Identify the blood parasite species.
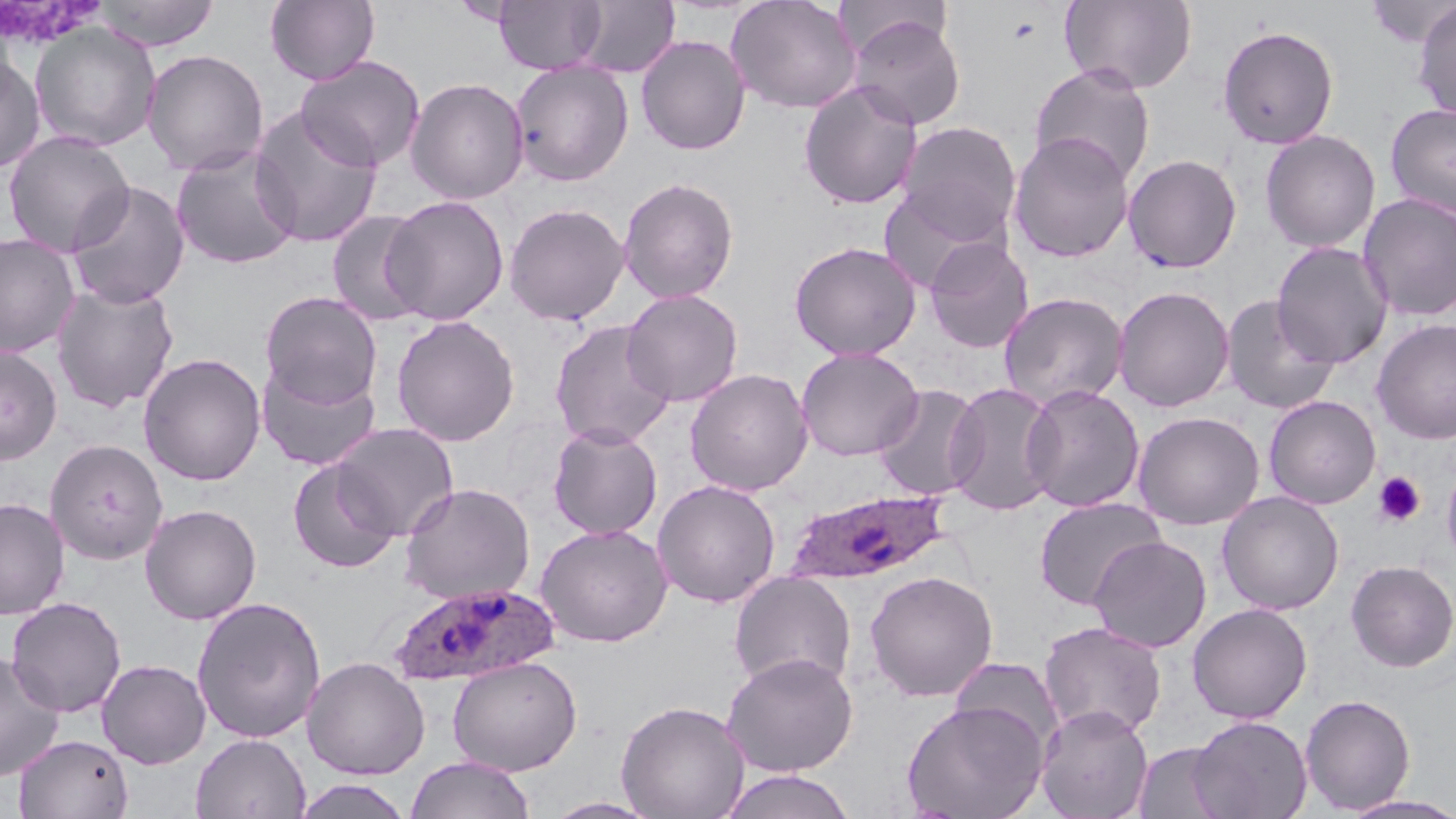
Plasmodium ovale.

{
  "field_of_view": "one of a larger specimen",
  "platelet_locations": "approximate bounding boxes as (x1,y1)-(x2,y2) corner pairs in pixels: (1373,472)-(1426,527)",
  "magnification": "1000x",
  "uninfected_red_blood_cell_locations": "approximate bounding boxes as (x1,y1)-(x2,y2) corner pairs in pixels: (92,0)-(220,51), (265,0)-(380,85), (493,0)-(607,75), (575,0)-(679,78), (726,0)-(861,114), (1363,0)-(1455,48), (1060,1)-(1198,94), (1413,3)-(1456,121), (846,13)-(966,130), (30,22)-(161,152), (1217,25)-(1339,149), (636,35)-(750,155), (141,49)-(269,177), (0,54)-(46,175), (296,55)-(426,172), (510,60)-(635,186), (1030,63)-(1156,186), (405,77)-(529,204), (798,80)-(923,210), (1384,103)-(1456,218), (249,108)-(382,248), (897,121)-(1021,242), (1,130)-(136,258), (1260,130)-(1381,253), (1008,131)-(1135,262), (170,145)-(300,270), (1123,153)-(1242,273), (618,176)-(739,304), (66,181)-(190,309), (877,186)-(1005,295), (1358,193)-(1456,322), (381,195)-(509,325), (504,202)-(629,326), (327,210)-(432,326), (0,233)-(81,358), (923,237)-(1034,353), (789,241)-(921,360), (1271,241)-(1393,368), (51,282)-(179,413), (1112,285)-(1235,412), (621,289)-(743,407), (259,291)-(382,408), (998,292)-(1128,411), (1220,295)-(1341,415), (390,315)-(520,447), (1371,318)-(1456,444), (549,320)-(677,450), (0,345)-(62,465), (795,346)-(923,461), (138,352)-(266,486), (255,358)-(381,472), (684,368)-(813,496), (944,381)-(1061,517), (873,383)-(985,501), (1021,384)-(1145,512), (1264,395)-(1382,509), (1132,410)-(1265,530), (330,423)-(459,540), (547,423)-(663,540), (46,439)-(168,564), (287,458)-(401,574), (1442,459)-(1456,565), (651,479)-(781,608), (399,482)-(535,604), (1217,490)-(1344,615), (0,497)-(69,620), (1033,497)-(1167,611), (139,503)-(262,625), (535,523)-(672,647), (1089,535)-(1211,653), (1345,560)-(1456,672), (729,570)-(857,693), (864,570)-(999,702), (5,596)-(127,718), (190,596)-(326,743), (1187,603)-(1312,723), (1038,621)-(1167,740), (0,650)-(65,782), (721,652)-(859,777), (447,655)-(582,775), (301,656)-(430,780), (948,656)-(1065,755), (97,659)-(211,769), (1299,694)-(1416,814), (616,699)-(750,819), (901,699)-(1049,819), (1035,703)-(1154,819), (1189,715)-(1312,819), (14,733)-(134,818), (190,733)-(311,819), (1132,741)-(1233,819), (406,755)-(535,819), (717,769)-(857,819), (291,778)-(415,819), (1338,793)-(1456,818), (543,797)-(662,818)",
  "modality": "optical microscopy",
  "stain": "May-Grünwald-Giemsa",
  "image_size": "1456×819 pixels",
  "plasmodium_ovale_infected_red_blood_cell_locations": "approximate bounding boxes as (x1,y1)-(x2,y2) corner pairs in pixels: (784,488)-(952,588), (389,582)-(558,687)",
  "preparation": "thin blood film"
}